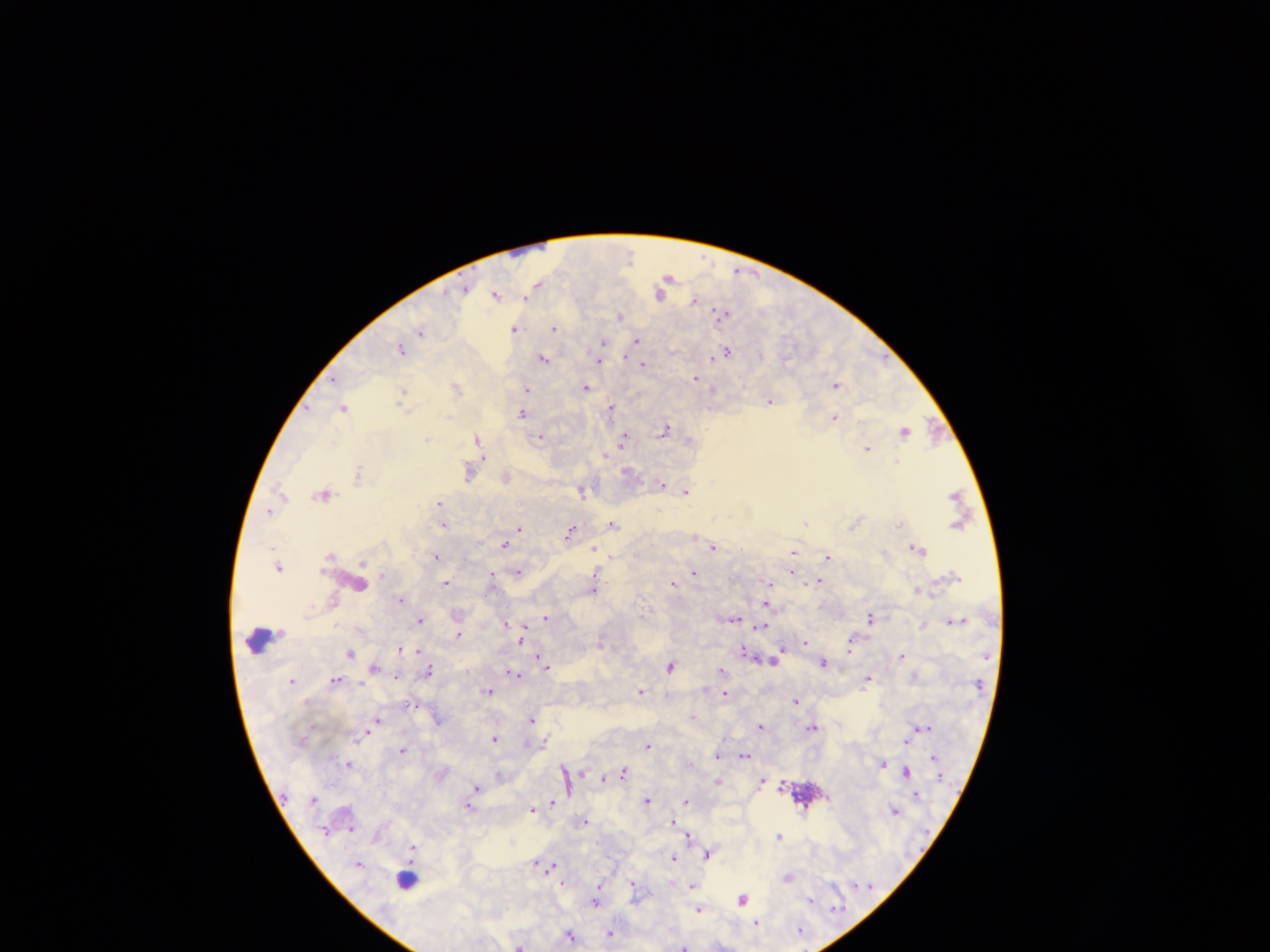
Approximate centers as [x, y] in pixels. Leukocyte locations: [261, 641], [406, 878]. Plasmodium parasite locations: [669, 275], [541, 284], [465, 290], [497, 294], [660, 296], [528, 297], [695, 298], [723, 313], [621, 316], [553, 328], [514, 329], [421, 335], [636, 341], [604, 343], [636, 345], [401, 349], [725, 352], [712, 356], [544, 358], [600, 362], [643, 363], [694, 376], [837, 385], [585, 386], [458, 387], [528, 389], [403, 392], [771, 402], [610, 407], [345, 408], [521, 414], [448, 417], [835, 417], [904, 431], [664, 432], [623, 433], [478, 436], [542, 437], [427, 439], [622, 439], [867, 448], [606, 454], [483, 458], [360, 472], [469, 474], [507, 475], [357, 478], [662, 484], [581, 491], [687, 492], [324, 495], [439, 501], [806, 524], [900, 524], [613, 525], [444, 526], [519, 528], [572, 531], [504, 545], [595, 547], [714, 548], [919, 549], [794, 551], [437, 558], [383, 575], [694, 576], [495, 577], [446, 582], [820, 582], [770, 583], [673, 584], [918, 590], [594, 591], [400, 599], [767, 606], [546, 616], [870, 617], [734, 620], [419, 622], [336, 625], [525, 628], [762, 628], [458, 635], [520, 639], [805, 642], [600, 643], [400, 648], [782, 649], [417, 651], [743, 651], [850, 651], [350, 653], [538, 655], [777, 655], [902, 655], [823, 663], [671, 666], [548, 668], [375, 669], [430, 669], [722, 670], [511, 672], [395, 676], [868, 677], [337, 678], [361, 684], [640, 690], [489, 691], [725, 694], [796, 700], [414, 706], [531, 718], [377, 719], [762, 725], [815, 726], [923, 726], [496, 739], [545, 740], [907, 740], [648, 747], [403, 750], [718, 756], [744, 756], [931, 757], [349, 764], [882, 764], [561, 766], [625, 770], [907, 770], [564, 772], [578, 772], [584, 772], [603, 777], [763, 781], [782, 782], [477, 788], [647, 800], [687, 801], [550, 803], [470, 807], [531, 811], [584, 823], [671, 823], [351, 829], [781, 836], [688, 838], [412, 848], [708, 854], [673, 859], [359, 862], [535, 862], [551, 866], [598, 884], [632, 884], [833, 885], [693, 886], [633, 891], [811, 897], [741, 899], [814, 901], [597, 903], [836, 906], [700, 909], [757, 922], [610, 932], [570, 934], [520, 943], [685, 944]. Photographed through a microscope with a mobile-phone camera. Single field of view. Image is 1270×952 pixels. Collected in Ghana. Thick blood film.